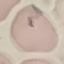
malaria status = uninfected
stain = Giemsa
preparation = thin blood smear
capture = smartphone camera at the microscope eyepiece
image type = automatically extracted cell patch, resized to 64 × 64 pixels